Locate every blood parasite and identify its species.
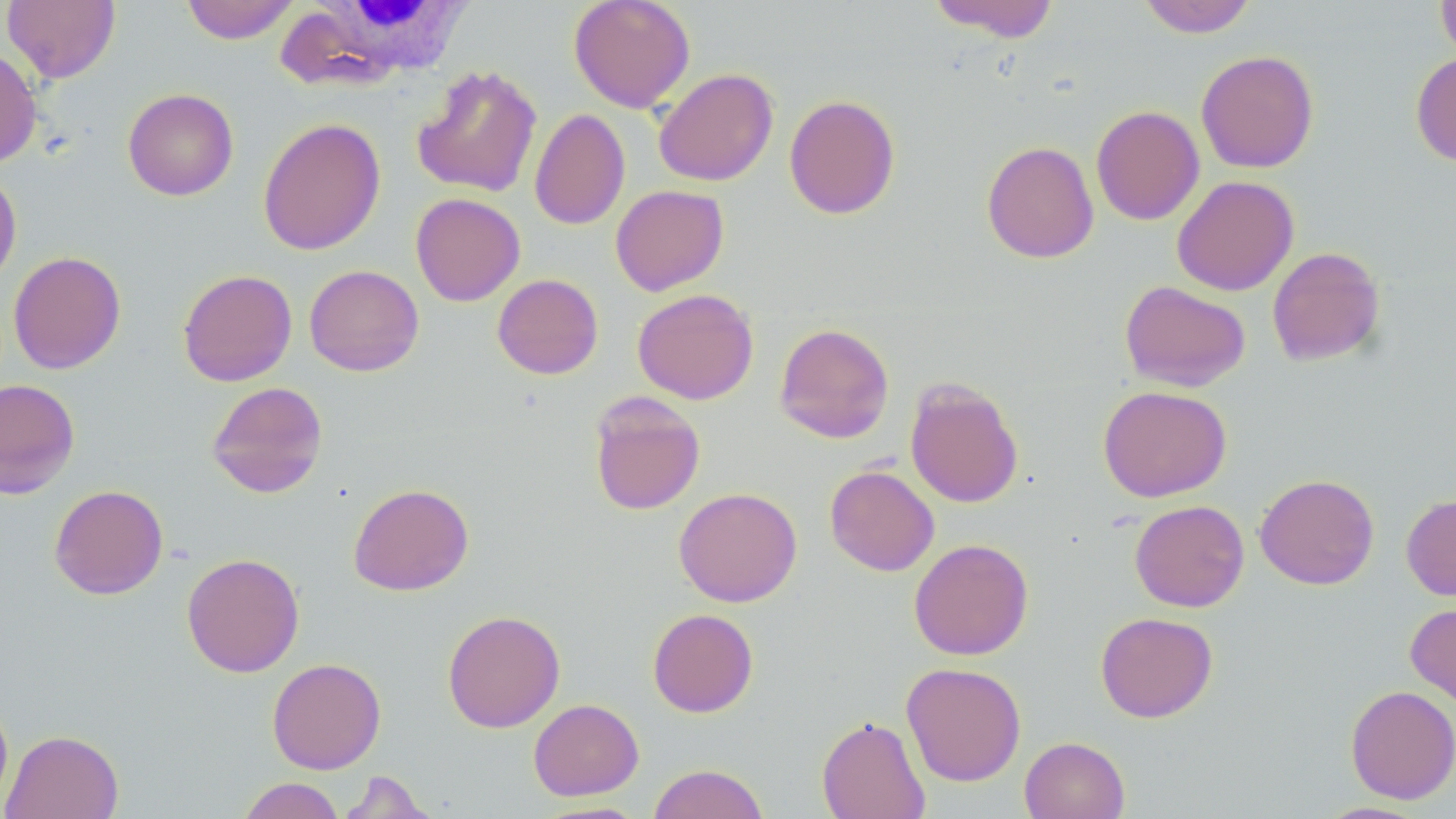
No blood parasites observed.

slide_level_diagnosis: no evidence of blood parasites
white_blood_cell_locations: 'approximate bounding boxes as (x1,y1)-(x2,y2) corner pairs in pixels: (276,0)-(478,89)'
uninfected_red_blood_cell_locations: 'approximate bounding boxes as (x1,y1)-(x2,y2) corner pairs in pixels: (3,0)-(120,83), (181,0)-(300,44), (568,0)-(696,113), (927,0)-(1060,42), (1137,0)-(1257,38), (1436,0)-(1456,64), (0,45)-(42,169), (1195,50)-(1319,173), (1410,52)-(1456,166), (411,64)-(542,198), (653,67)-(779,187), (123,88)-(239,201), (784,94)-(901,219), (1091,105)-(1205,225), (529,109)-(630,230), (258,117)-(385,256), (981,140)-(1100,264), (0,169)-(22,288), (1171,175)-(1299,296), (610,185)-(729,296), (410,193)-(525,306), (1266,246)-(1386,367), (8,250)-(126,374), (304,264)-(424,376), (177,268)-(298,387), (492,274)-(603,380), (1120,279)-(1251,391), (632,288)-(759,405), (774,322)-(895,444), (0,378)-(80,499), (905,378)-(1024,509), (206,381)-(328,498), (1098,385)-(1231,502), (588,392)-(706,515), (824,465)-(939,576), (1254,473)-(1380,590), (348,483)-(474,596), (49,484)-(168,600), (673,487)-(802,607), (1401,493)-(1456,601), (1129,499)-(1250,612), (908,538)-(1034,660), (181,552)-(305,678), (1405,601)-(1456,708), (647,608)-(759,717), (442,609)-(565,733), (1095,612)-(1218,723), (266,657)-(386,774), (901,662)-(1026,786), (1345,685)-(1456,804), (0,694)-(13,810), (528,698)-(644,800), (817,715)-(930,819), (2,729)-(123,819), (1019,736)-(1130,819), (648,763)-(769,819), (337,770)-(436,818), (238,777)-(345,819), (533,801)-(650,818)'
field_of_view: one of a larger specimen
modality: light microscopy
stain: May-Grünwald-Giemsa
image_size: 1456×819 pixels
magnification: 1000x
preparation: thin blood smear